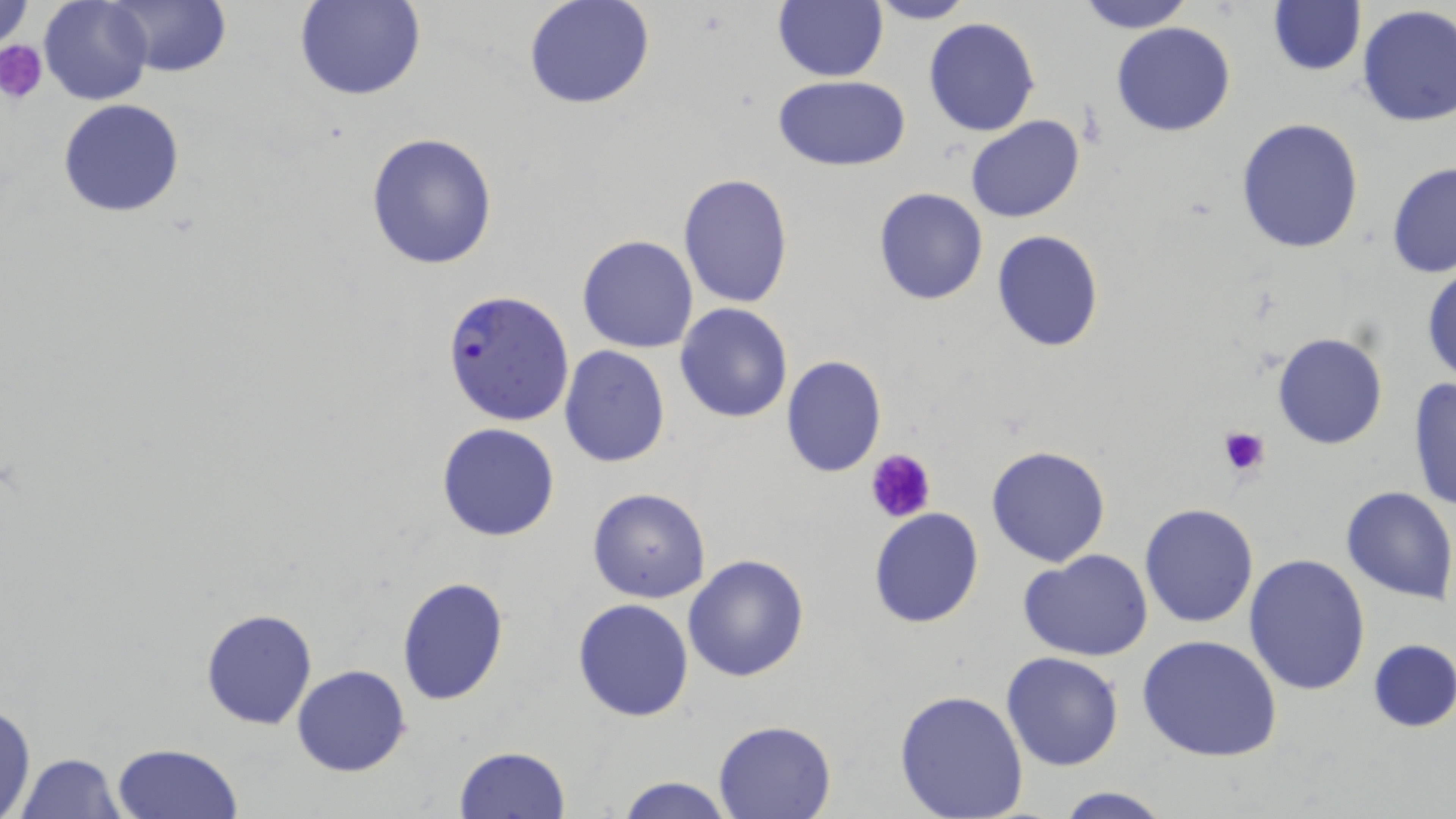
Summary:
  - Coordinate format: approximate bounding boxes as (x1,y1)-(x2,y2) corner pairs in pixels
  - Uninfected red blood cell locations: (39,0)-(154,105), (295,0)-(425,101), (523,0)-(656,110), (773,0)-(888,82), (866,0)-(975,25), (1074,0)-(1196,33), (1267,0)-(1366,75), (106,2)-(232,78), (1,4)-(32,52), (1355,5)-(1455,127), (922,18)-(1040,137), (1111,21)-(1236,136), (772,75)-(911,170), (58,99)-(186,218), (965,116)-(1086,222), (1235,118)-(1364,255), (364,131)-(499,270), (1386,162)-(1456,278), (677,174)-(793,308), (872,187)-(988,306), (991,229)-(1104,353), (576,234)-(700,353), (1422,263)-(1455,385), (675,303)-(793,423), (1271,332)-(1388,451), (559,345)-(670,468), (780,355)-(886,477), (1406,374)-(1456,516), (436,422)-(561,541), (986,445)-(1112,566), (1340,485)-(1455,603), (586,487)-(711,603), (1139,502)-(1258,628), (868,508)-(985,629), (1019,550)-(1154,661), (1243,552)-(1370,695), (683,554)-(810,683), (395,575)-(511,706), (572,600)-(693,721), (201,607)-(318,730), (1137,634)-(1284,761), (1368,639)-(1456,732), (1001,652)-(1124,771), (292,663)-(411,777), (894,689)-(1029,818), (1,700)-(37,819), (712,719)-(839,818), (110,742)-(244,819), (453,746)-(572,819), (12,752)-(128,818), (612,776)-(736,818), (1051,786)-(1171,819)
  - Plasmodium falciparum-infected red blood cell locations: (442,288)-(576,427)
  - Platelet locations: (0,39)-(49,103), (1217,425)-(1271,478), (865,449)-(937,525)
  - Slide-level diagnosis: Plasmodium falciparum
  - Image size: 1456×819 pixels
  - Preparation: thin blood film
  - Field of view: single
  - Modality: light microscopy
  - Magnification: 1000x
  - Stain: May-Grünwald-Giemsa